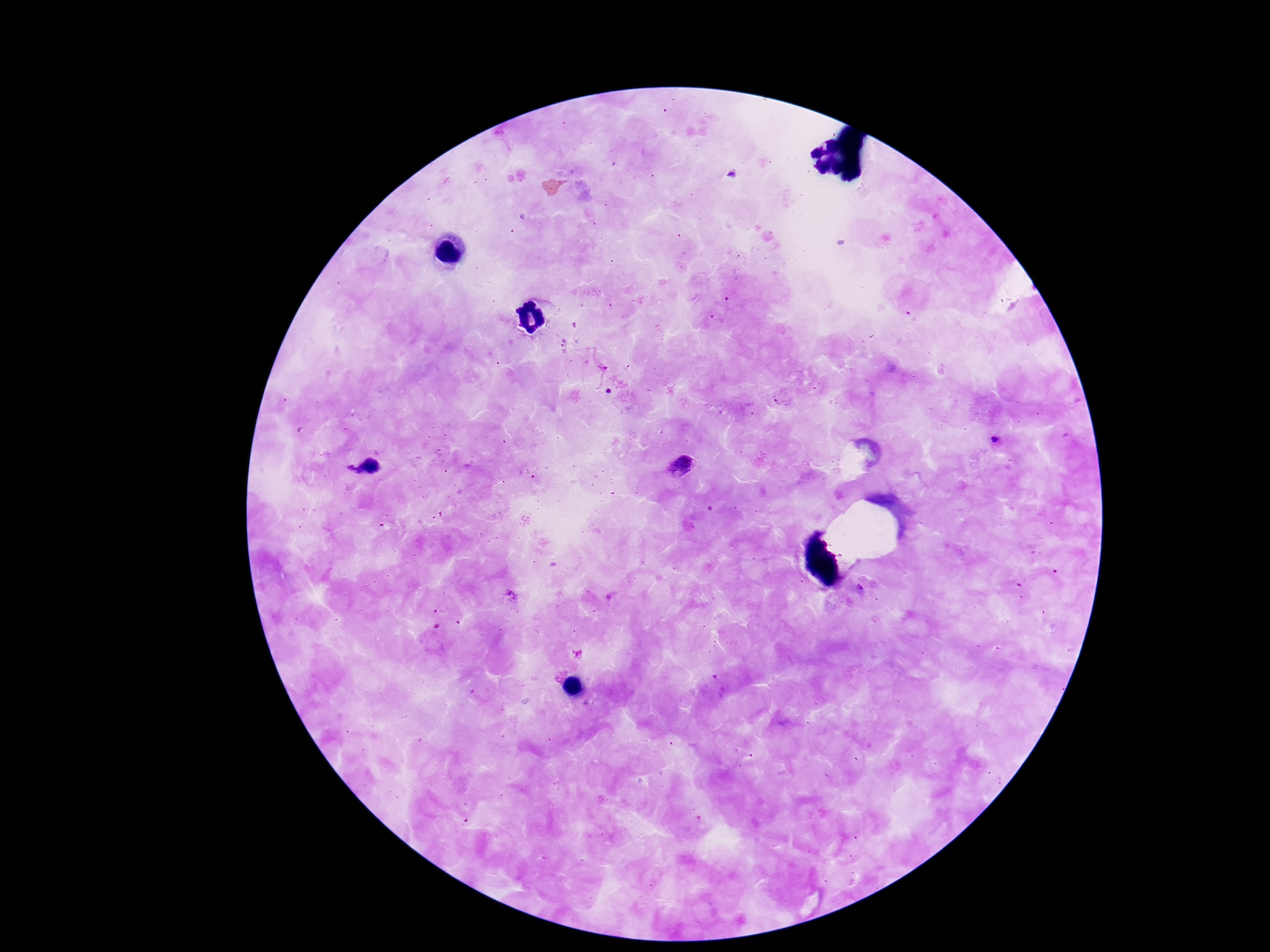

preparation: thick blood smear
stain: Giemsa
patient_malaria_status: infected
capture: smartphone camera through the microscope eyepiece
field_of_view: one from this slide
magnification: 100x
image_size: 1270×952 pixels
plasmodium_parasite_locations: 'approximate centers as (x, y) in pixels: (1002, 442), (686, 465), (368, 469)'